Classify this cell by malaria status.
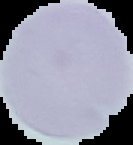
Uninfected.

image type = cell region segmented out of the field of view; surrounding area masked to black
image size = 133×145 pixels
preparation = thin blood film